Locate and identify every blood parasite.
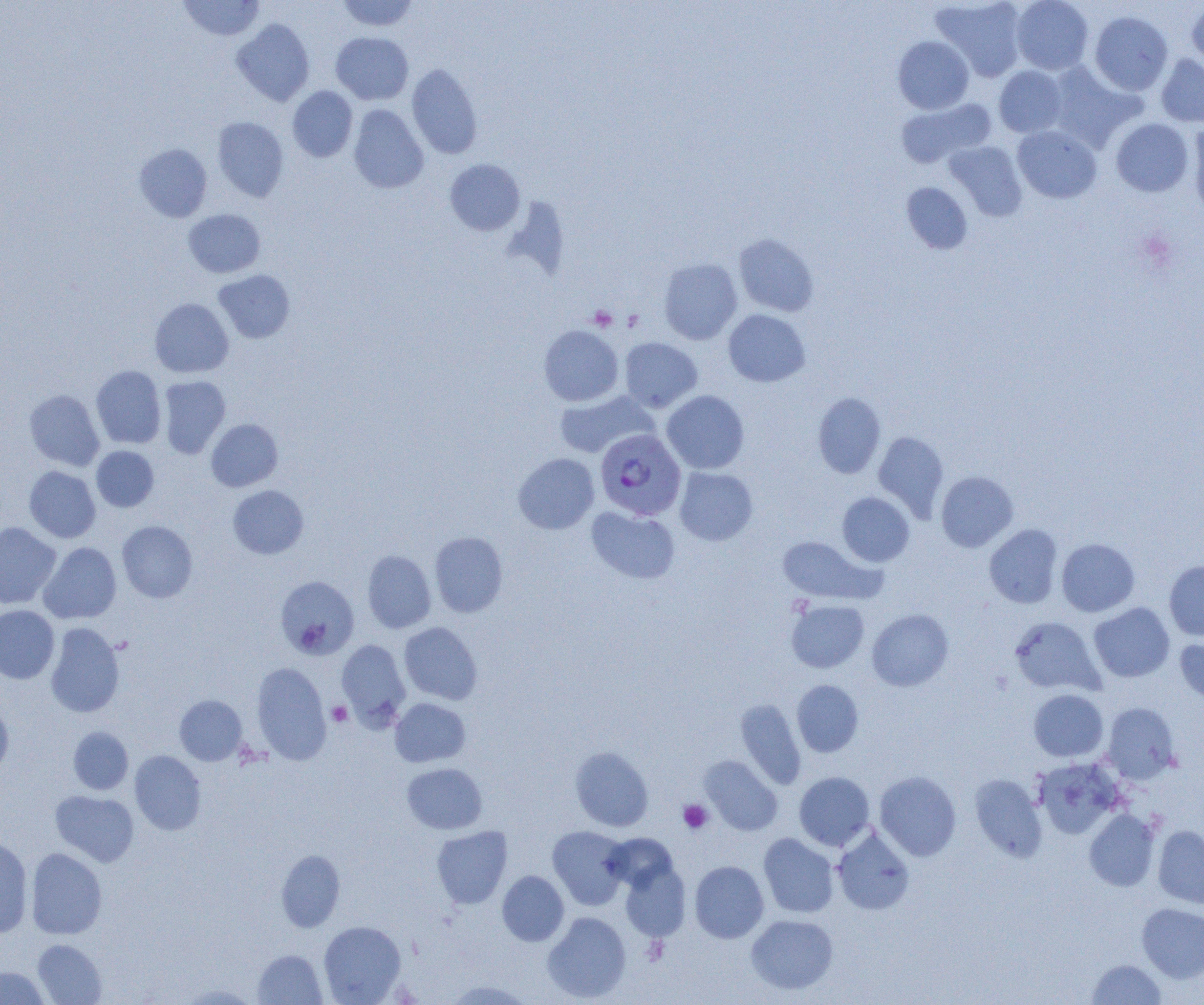

Approximate bounding boxes as [x1, y1, x2, y2] in pixels.
Plasmodium falciparum-infected red blood cells: [595, 428, 686, 520].
No Plasmodium ovale, Plasmodium malariae, Plasmodium vivax, Babesia divergens, or Trypanosoma brucei observed.

slide-level diagnosis = Plasmodium falciparum
modality = optical microscopy
platelet locations = approximate bounding boxes as [x1, y1, x2, y2] in pixels: [588, 306, 617, 331], [328, 701, 352, 726], [678, 799, 713, 833], [642, 935, 669, 965]
field of view = single
image size = 1204×1005 pixels
uninfected red blood cell locations = approximate bounding boxes as [x1, y1, x2, y2] in pixels: [177, 0, 265, 41], [336, 0, 419, 32], [931, 0, 1027, 81], [1011, 0, 1094, 75], [1186, 2, 1204, 72], [1089, 11, 1173, 95], [232, 19, 315, 106], [331, 32, 414, 105], [893, 36, 974, 114], [1156, 54, 1204, 127], [1045, 62, 1142, 152], [407, 63, 483, 159], [994, 66, 1066, 138], [288, 86, 357, 162], [897, 97, 995, 167], [348, 105, 428, 193], [212, 117, 289, 202], [1111, 118, 1193, 196], [1188, 122, 1204, 218], [1012, 125, 1102, 203], [944, 140, 1027, 220], [134, 143, 212, 222], [445, 159, 525, 235], [901, 182, 972, 254], [183, 209, 266, 277], [734, 234, 818, 317], [658, 258, 742, 344], [213, 270, 295, 342], [150, 298, 233, 378], [723, 310, 810, 386], [539, 325, 623, 406], [619, 337, 702, 412], [91, 365, 166, 449], [158, 376, 231, 459], [24, 389, 104, 471], [662, 390, 749, 473], [555, 391, 657, 458], [813, 392, 885, 478], [206, 419, 283, 491], [873, 431, 949, 519], [91, 446, 159, 512], [513, 453, 599, 534], [24, 466, 100, 543], [674, 467, 758, 546], [936, 471, 1018, 552], [228, 485, 308, 559], [837, 492, 914, 566], [586, 506, 680, 584], [117, 521, 197, 603], [0, 522, 61, 609], [984, 525, 1063, 608], [429, 531, 508, 617], [777, 536, 876, 604], [1056, 538, 1140, 616], [38, 542, 121, 624], [362, 550, 436, 633], [1164, 560, 1204, 641], [276, 576, 359, 660], [786, 599, 869, 673], [1089, 602, 1175, 682], [0, 605, 59, 684], [787, 605, 953, 678], [867, 609, 953, 691], [1009, 616, 1103, 696], [399, 622, 482, 704], [45, 623, 125, 717], [1175, 638, 1204, 707], [337, 639, 410, 728], [251, 662, 331, 764], [791, 680, 863, 757], [1029, 690, 1108, 762], [175, 695, 247, 765], [390, 698, 470, 767], [735, 699, 806, 789], [0, 700, 13, 780], [1101, 702, 1180, 784], [68, 727, 134, 794], [570, 746, 653, 831], [129, 750, 206, 835], [699, 755, 782, 835], [1033, 758, 1124, 839], [402, 762, 487, 834], [875, 771, 962, 861], [794, 772, 874, 850], [970, 774, 1048, 861], [50, 790, 139, 867], [1084, 809, 1160, 891], [832, 825, 915, 915], [1153, 825, 1204, 909], [432, 826, 512, 909], [547, 826, 631, 910], [759, 833, 839, 918], [0, 837, 33, 937], [26, 848, 107, 939], [276, 849, 345, 932], [619, 859, 691, 942], [689, 861, 768, 943], [497, 870, 569, 946], [1137, 903, 1203, 982], [542, 912, 631, 1002], [746, 914, 838, 994], [319, 921, 406, 1004], [32, 939, 107, 1004], [252, 949, 326, 1004], [1086, 959, 1166, 1004], [0, 966, 50, 1004], [445, 979, 534, 1004], [178, 984, 261, 1004]
magnification = 1000x
preparation = thin blood film